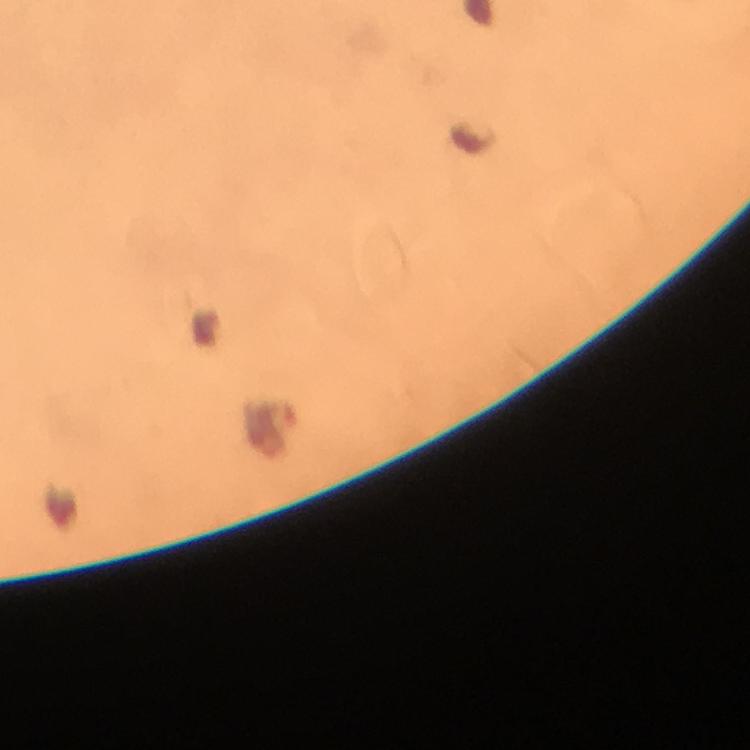
Approximate centers as {x, y} in pixels.
Summary:
  - Plasmodium parasite locations: {271, 430}
  - Cropped from: a single field of view
  - Immersion oil: used
  - Stain: Giemsa
  - Preparation: thick blood film
  - Image size: 750×750 pixels
  - Magnification: 100x
  - Context: from a diagnostic examination for malaria
  - Capture: smartphone photograph through a microscope